Name the parasite shown.
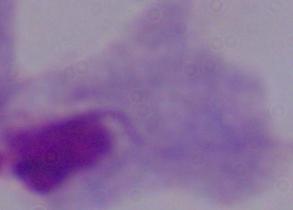
A trichomonad.

Photomicrograph. Captured at 1000x magnification.